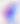
identification = Toxoplasma gondii
magnification = 400x
modality = photomicrograph